Assess this cell for malaria.
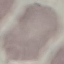
Uninfected.

Cell patch, automatically extracted from a larger field of view and resized to 64 × 64 pixels. Thin blood smear. Acquired by smartphone through the microscope eyepiece. Giemsa stain.